Point out each malaria parasite.
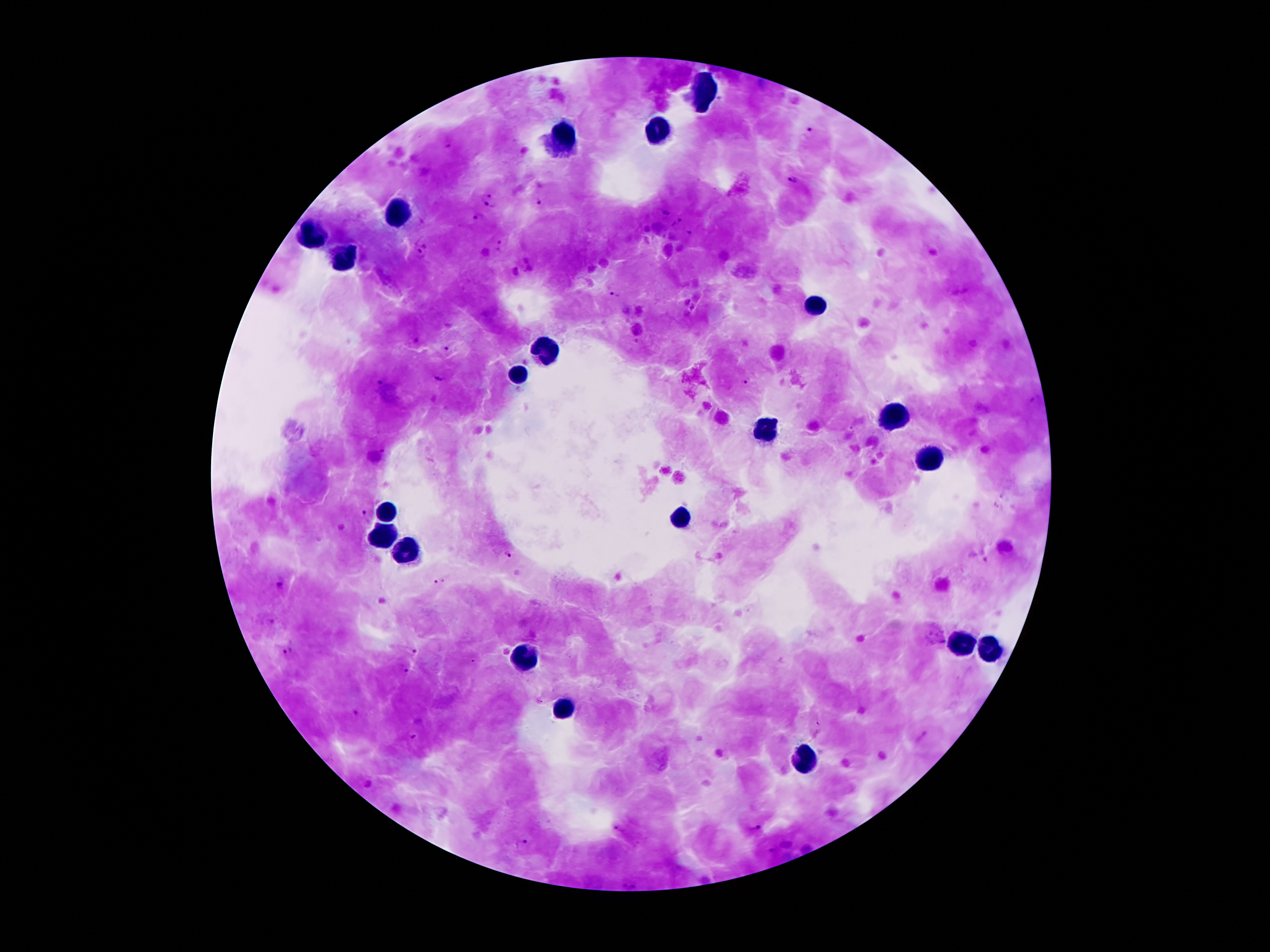

Approximate centers as [x, y] in pixels.
Malaria parasites: [808, 132], [445, 142], [794, 181], [489, 200], [538, 202], [661, 213], [476, 219], [679, 221], [688, 232], [423, 239], [500, 245], [420, 255], [613, 293], [416, 339], [448, 347], [440, 376], [745, 381], [378, 383], [1034, 400], [363, 515], [504, 555], [279, 581], [438, 581], [410, 651], [288, 654], [403, 670], [354, 714], [410, 736], [618, 827], [752, 827], [521, 844], [772, 848], [629, 884].

preparation: thick peripheral-blood smear
field_of_view: single
capture: smartphone through the microscope eyepiece
patient_malaria_status: infected with Plasmodium falciparum
stain: Giemsa
leukocyte_locations: 'approximate centers as [x, y] in pixels: [707, 91], [656, 133], [563, 136], [399, 212], [314, 236], [344, 258], [815, 308], [550, 350], [518, 373], [891, 416], [764, 430], [929, 461], [390, 514], [682, 521], [382, 536], [411, 550], [958, 637], [988, 651], [526, 655], [560, 709], [805, 758]'
magnification: 100x
image_size: 1270×952 pixels